Point out Plasmodium parasites and leukocytes.
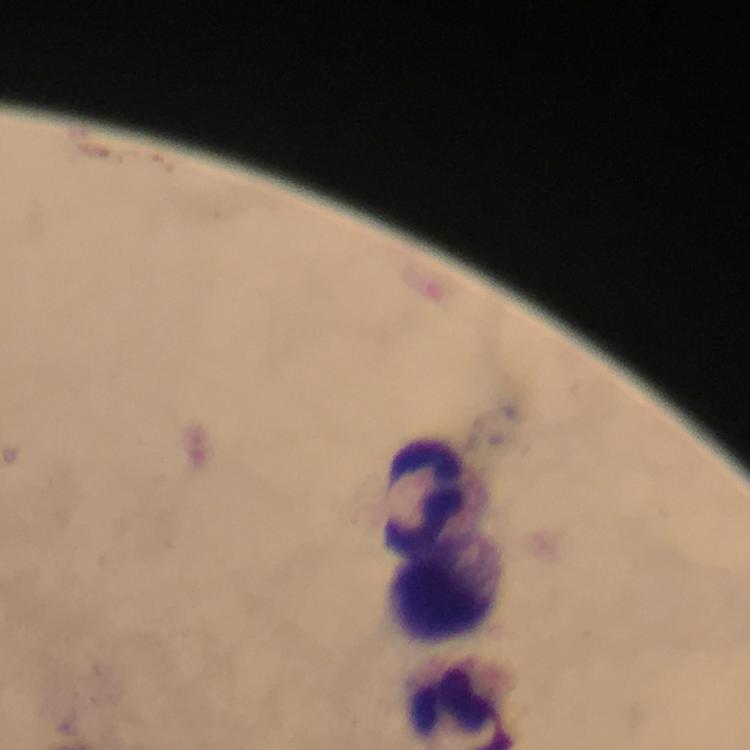

No Plasmodium parasites detected.
Approximate centers as {x, y} in pixels.
Leukocytes: {424, 490}, {447, 579}.

context = from a diagnostic examination for malaria
image size = 750×750 pixels
preparation = thick smear
magnification = 100x
immersion oil = used
stain = Giemsa
capture = smartphone mounted on the microscope
cropped from = one field of view